Point out every Plasmodium parasite and every leukocyte.
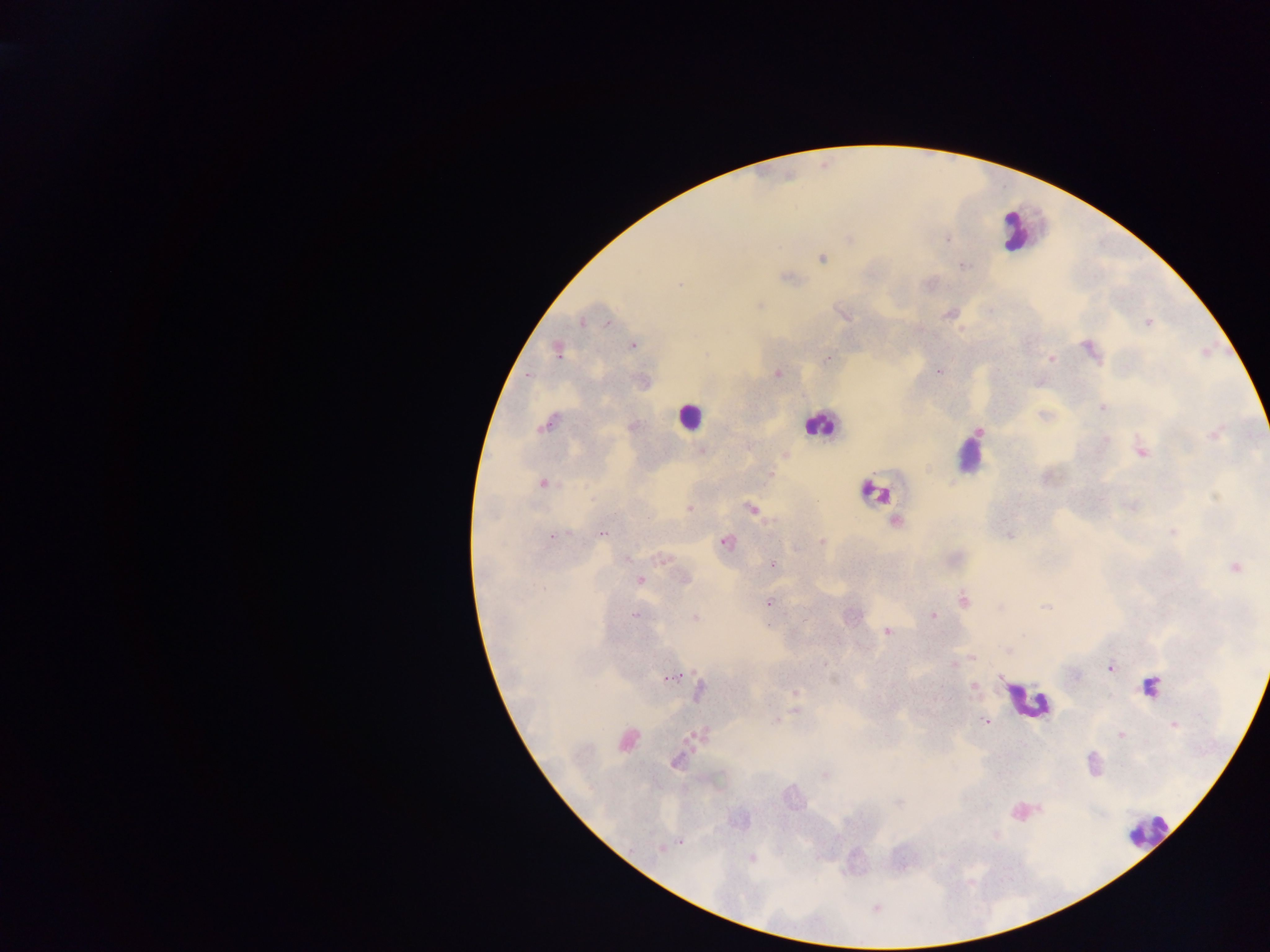

Approximate centers as [x, y] in pixels.
Plasmodium parasites: [947, 239], [822, 258], [964, 266], [786, 278], [679, 284], [759, 305], [949, 314], [844, 315], [582, 322], [1148, 322], [607, 323], [633, 346], [1089, 348], [558, 351], [827, 359], [1052, 359], [938, 372], [777, 373], [1102, 408], [546, 424], [979, 432], [1214, 435], [1106, 438], [702, 450], [1141, 452], [785, 455], [770, 474], [543, 483], [1216, 498], [1132, 505], [688, 509], [751, 509], [895, 521], [1173, 531], [569, 532], [603, 533], [1010, 535], [552, 536], [725, 541], [822, 541], [626, 558], [662, 558], [772, 565], [1235, 567], [640, 580], [685, 580], [964, 600], [768, 603], [999, 607], [1045, 607], [852, 615], [933, 615], [635, 616], [695, 617], [887, 631], [1008, 651], [973, 657], [954, 664], [1111, 668], [672, 676], [1075, 676], [973, 686], [1150, 686], [699, 691], [795, 692], [796, 711], [1200, 715], [776, 720], [985, 721], [1174, 725], [701, 733], [1121, 735], [627, 740], [676, 761], [1092, 762], [824, 775], [899, 802], [680, 842], [660, 849], [751, 857].
Leukocytes: [1014, 232], [689, 416], [819, 425], [970, 460], [874, 492], [1025, 699], [1147, 830].

country: Ghana
preparation: thick blood film
image_size: 1270×952 pixels
field_of_view: single
capture: mobile-phone photograph through a microscope